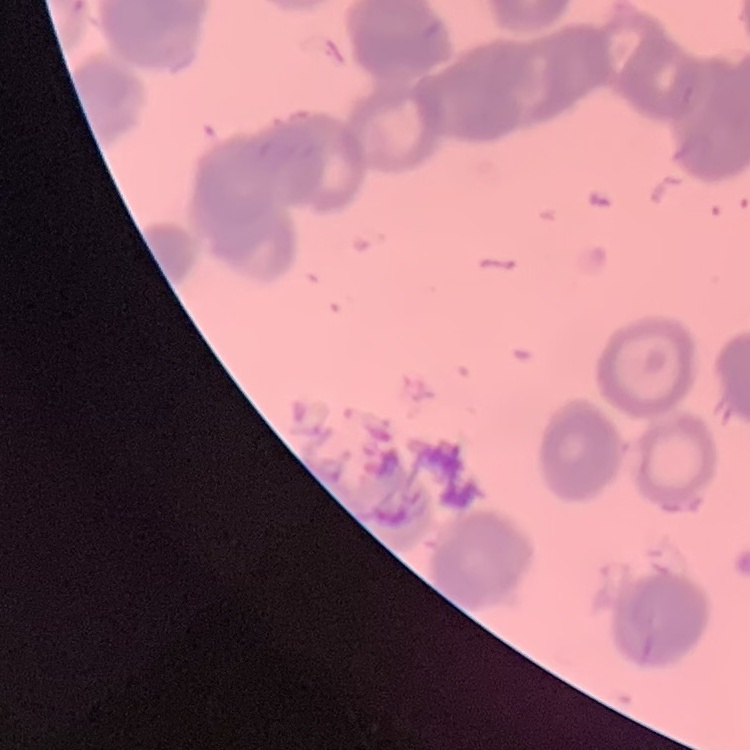 The erythrocytes show rouleaux formation. Stained with either Field's or Giemsa. Square crop of a larger photomicrograph. Thin blood film.